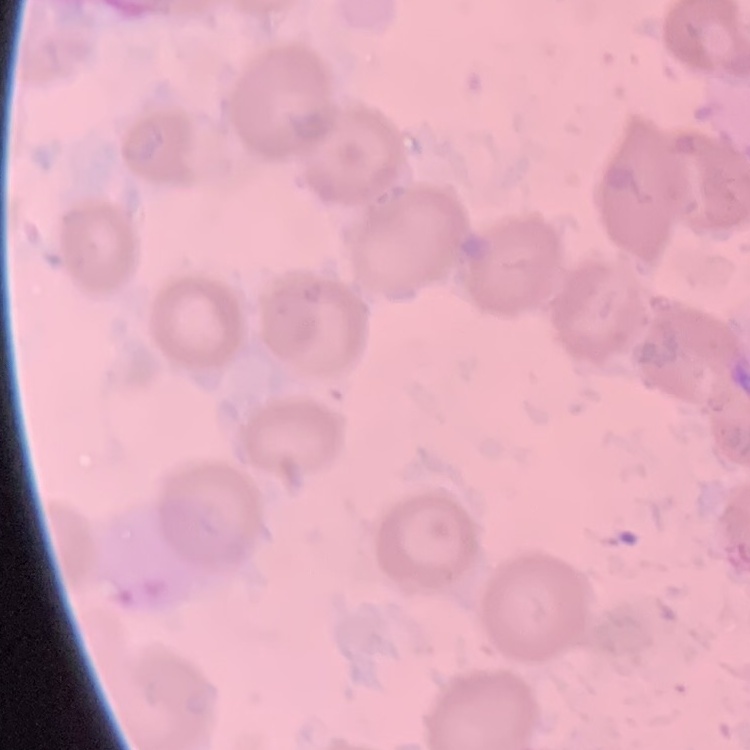
The red blood cells show no rouleaux formation. Square crop of a larger photomicrograph. Field's or Giemsa stain. Thin blood smear.